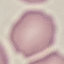 Result: no malaria parasites detected. Automatically extracted cell patch, resized to 64 × 64 pixels. Thin blood film. Acquired by smartphone through the microscope eyepiece. Giemsa stain.